Describe the morphology of the erythrocytes.
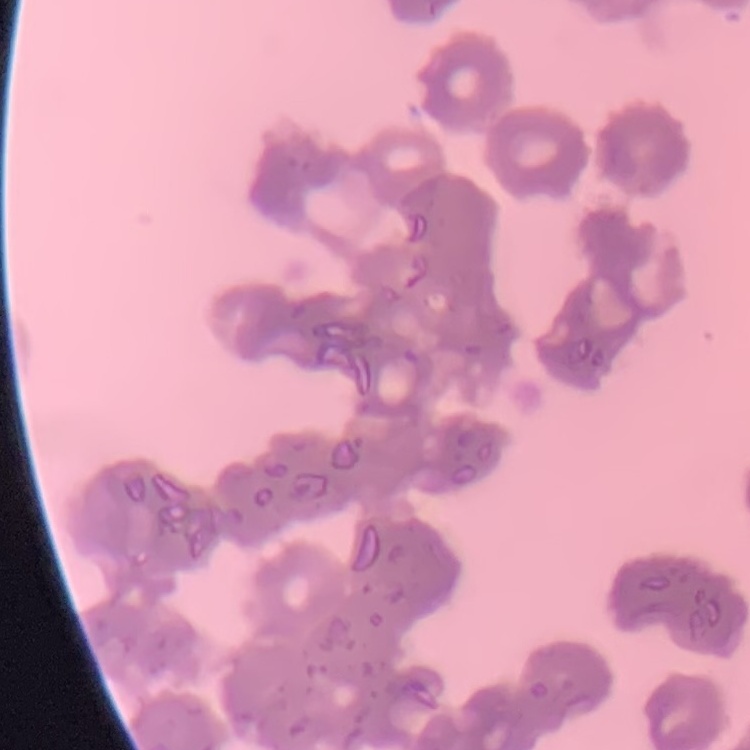

Rouleaux formation.

preparation = thin peripheral smear
image type = square crop of a larger photomicrograph
stain = Field's or Giemsa